Identify the parasite.
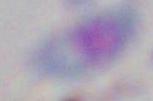
Toxoplasma gondii.

Summary:
  - Magnification: 1000x
  - Modality: photomicrograph